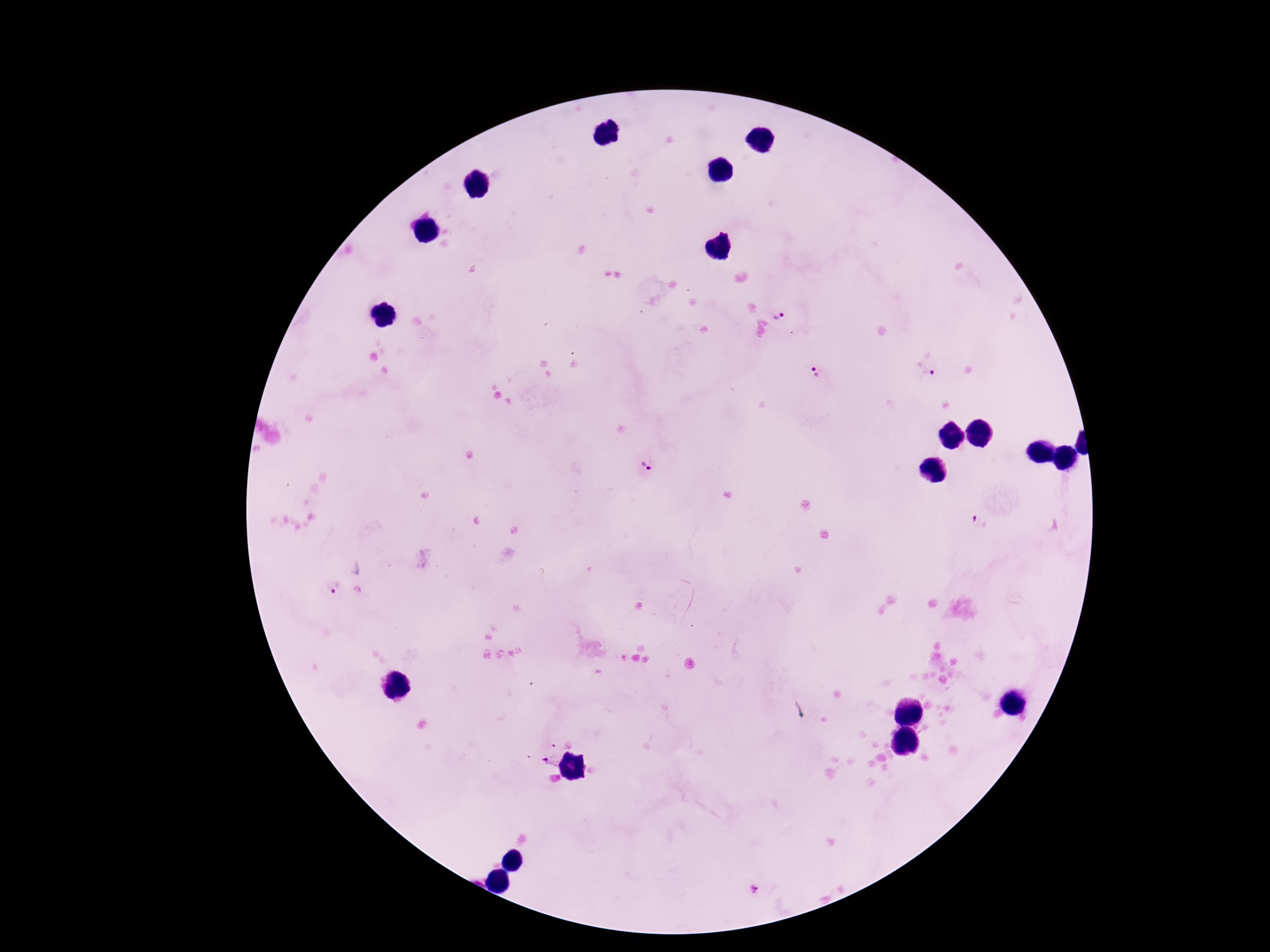

Approximate centers as [x, y] in pixels. Plasmodium parasite locations: [779, 314], [927, 368], [815, 371], [646, 467], [980, 520], [335, 587], [551, 760]. One field from this slide. Giemsa stain. Thick blood film. Patient malaria status: positive. 100x magnification. Image is 1270×952 pixels. Smartphone photograph taken through the microscope eyepiece.